Classify this cell by malaria status.
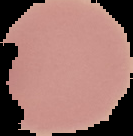

It is uninfected.

Cell region segmented out of the field of view; the surrounding area is masked to black. Image is 133×136 pixels. From a thin blood smear.